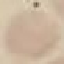

Summary:
  - Result: no malaria parasites seen
  - Image type: automatically extracted cell patch, resized to 64 × 64 pixels
  - Capture: smartphone through the microscope eyepiece
  - Stain: Giemsa
  - Preparation: thin blood smear